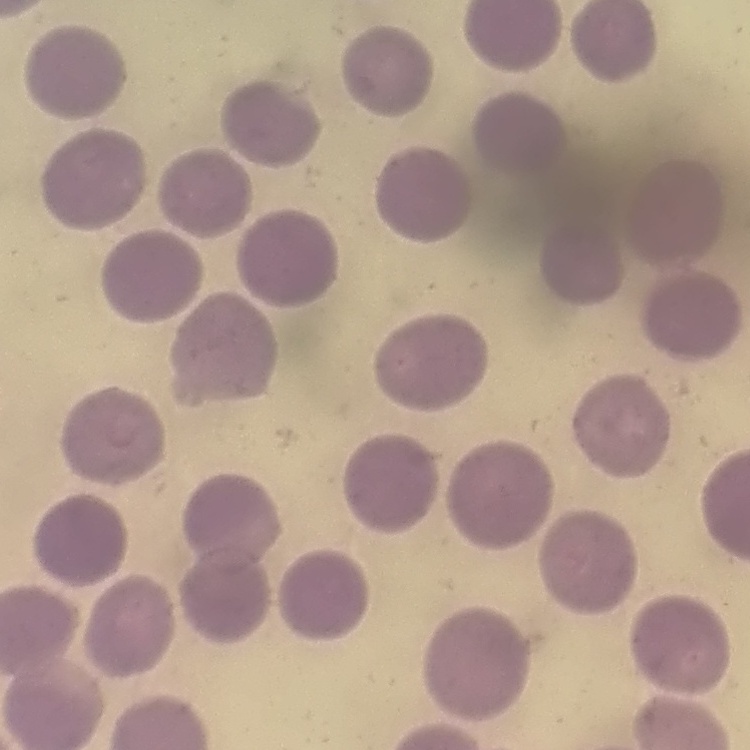

erythrocyte morphology = no rouleaux formation
preparation = thin blood film
stain = Field's or Giemsa
image type = square crop of a larger photomicrograph